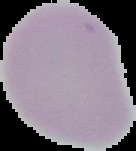
Summary:
  - Preparation: thin blood smear
  - Image size: 136×151 pixels
  - Result: negative for malaria parasites
  - Image type: cell region segmented out of the field of view; surrounding area masked to black